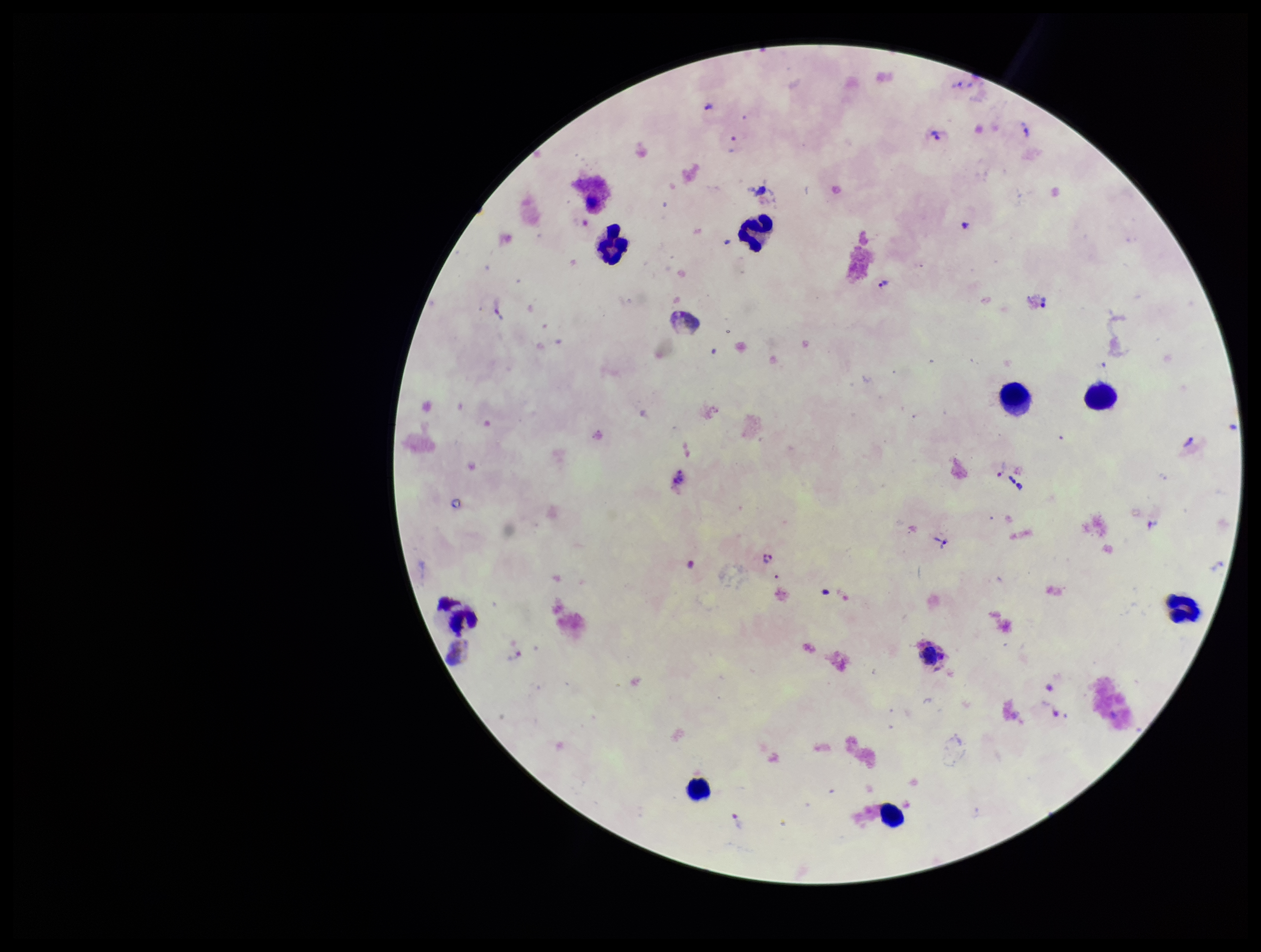 Leukocyte count: 9. Patient malaria status: infected. Stained with Giemsa. Image is 1261×952 pixels. Preparation: thick. Single field of view. Species reported for this patient: Plasmodium vivax. Plasmodium parasites: seen. Parasite count: 9. Smartphone photograph taken through the eyepiece of a microscope.